State the preparation type.
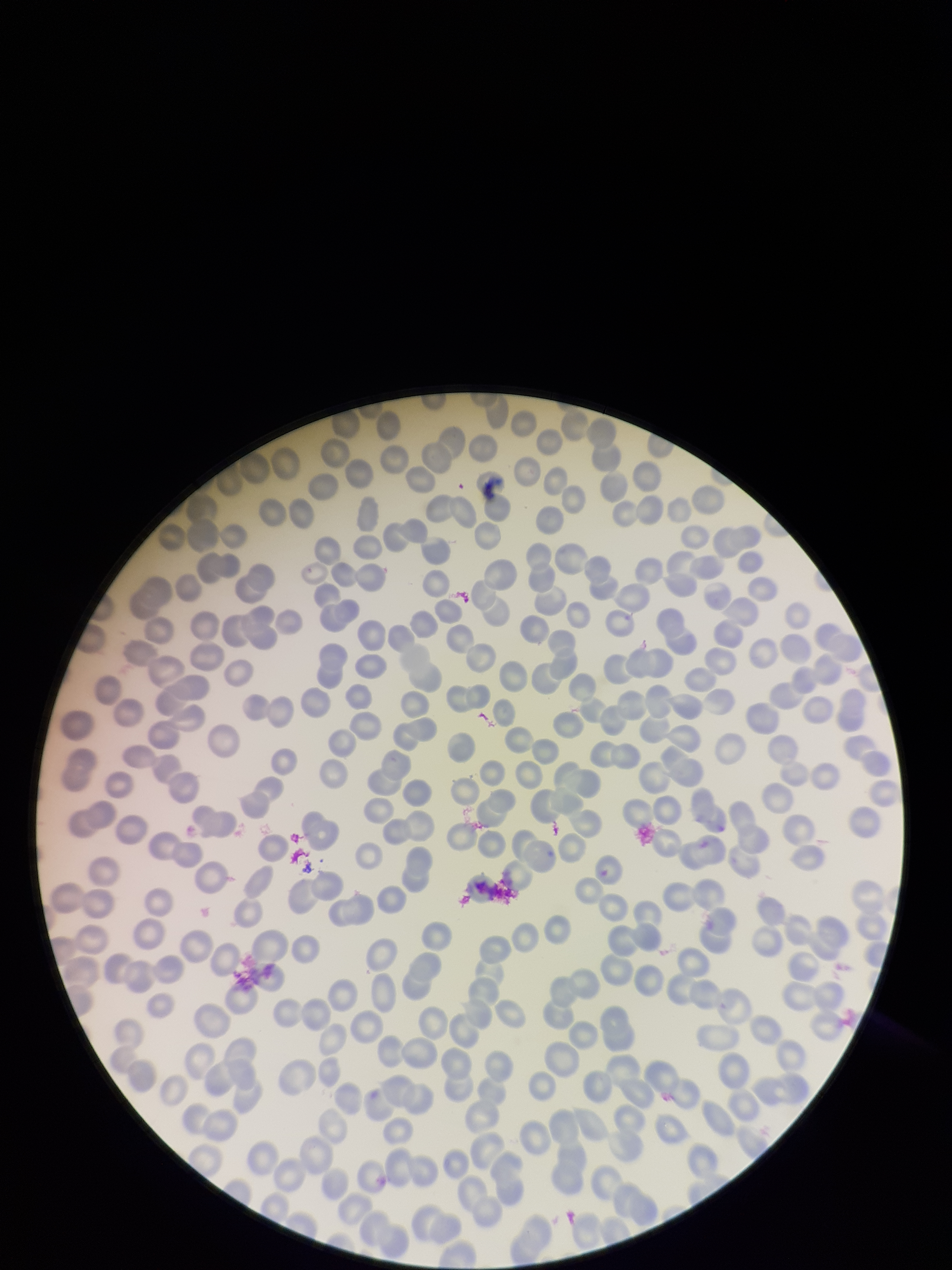

It is a thin blood smear.

Summary:
  - Image size: 952×1270 pixels
  - Parasitized red blood cells: none identified
  - Patient malaria status: negative
  - Stain: Giemsa
  - Parasitized red blood cell count: 0
  - Capture: smartphone photograph through the microscope eyepiece
  - Red blood cell count: 294
  - Field of view: single